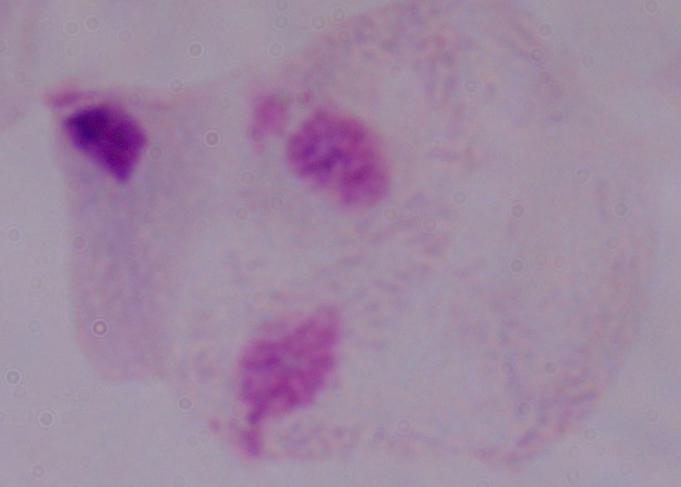

modality: photomicrograph
magnification: 1000x
identification: trichomonad